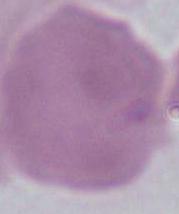

An erythrocyte is seen. 1000x magnification. Micrograph.